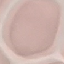

result = negative for malaria parasites
stain = Giemsa
preparation = thin smear
capture = smartphone camera at the microscope eyepiece
image type = cell patch, automatically extracted from a larger field of view and resized to 64 × 64 pixels